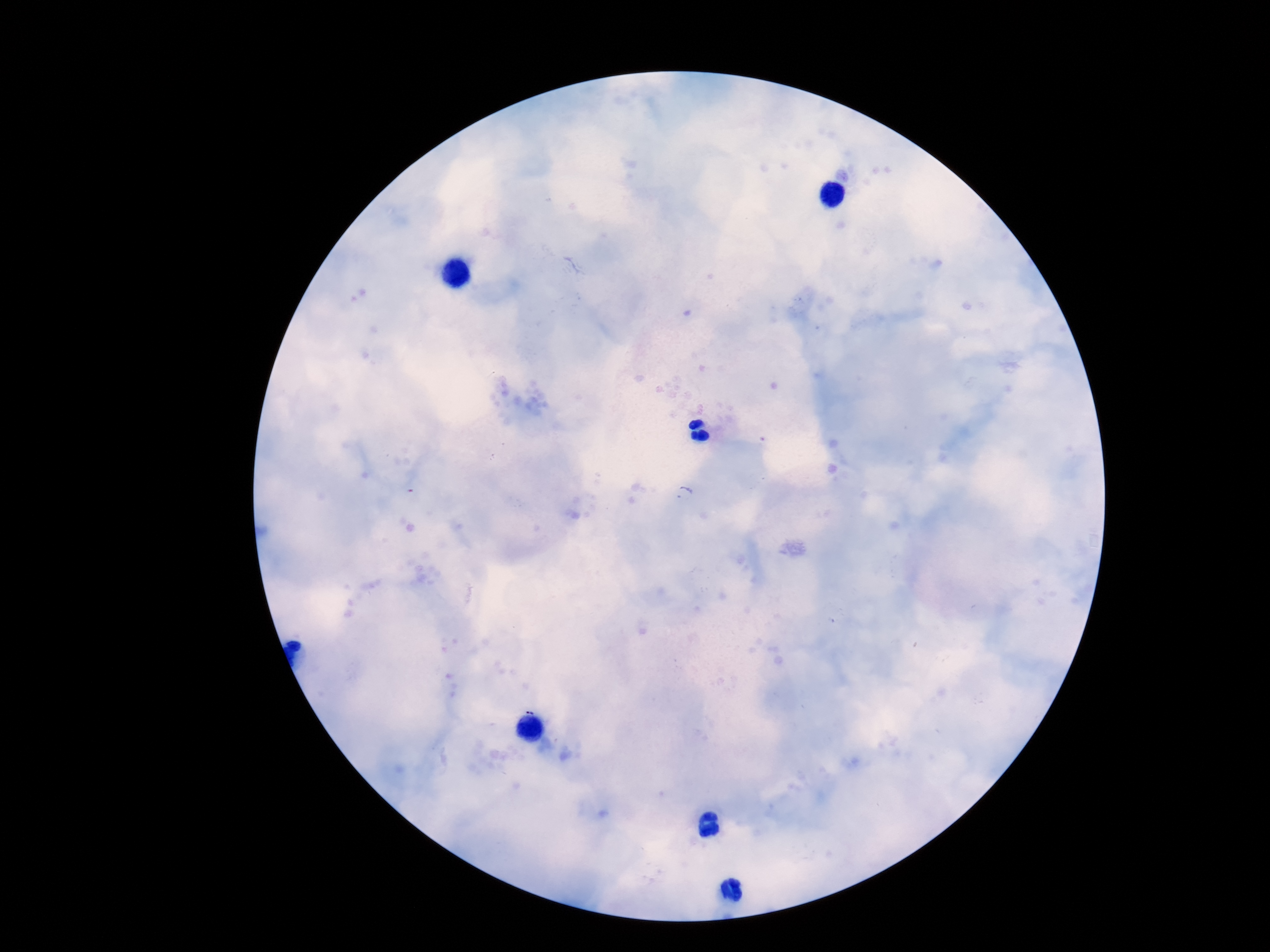

Approximate centers as {x, y} in pixels. Plasmodium parasite locations: {685, 494}, {530, 699}. 100x magnification. Patient malaria status: positive. One field from this slide. Smartphone photograph taken through the microscope eyepiece. Thick blood film. Giemsa stain. Image is 1270×952 pixels.